Point out each Plasmodium parasite.
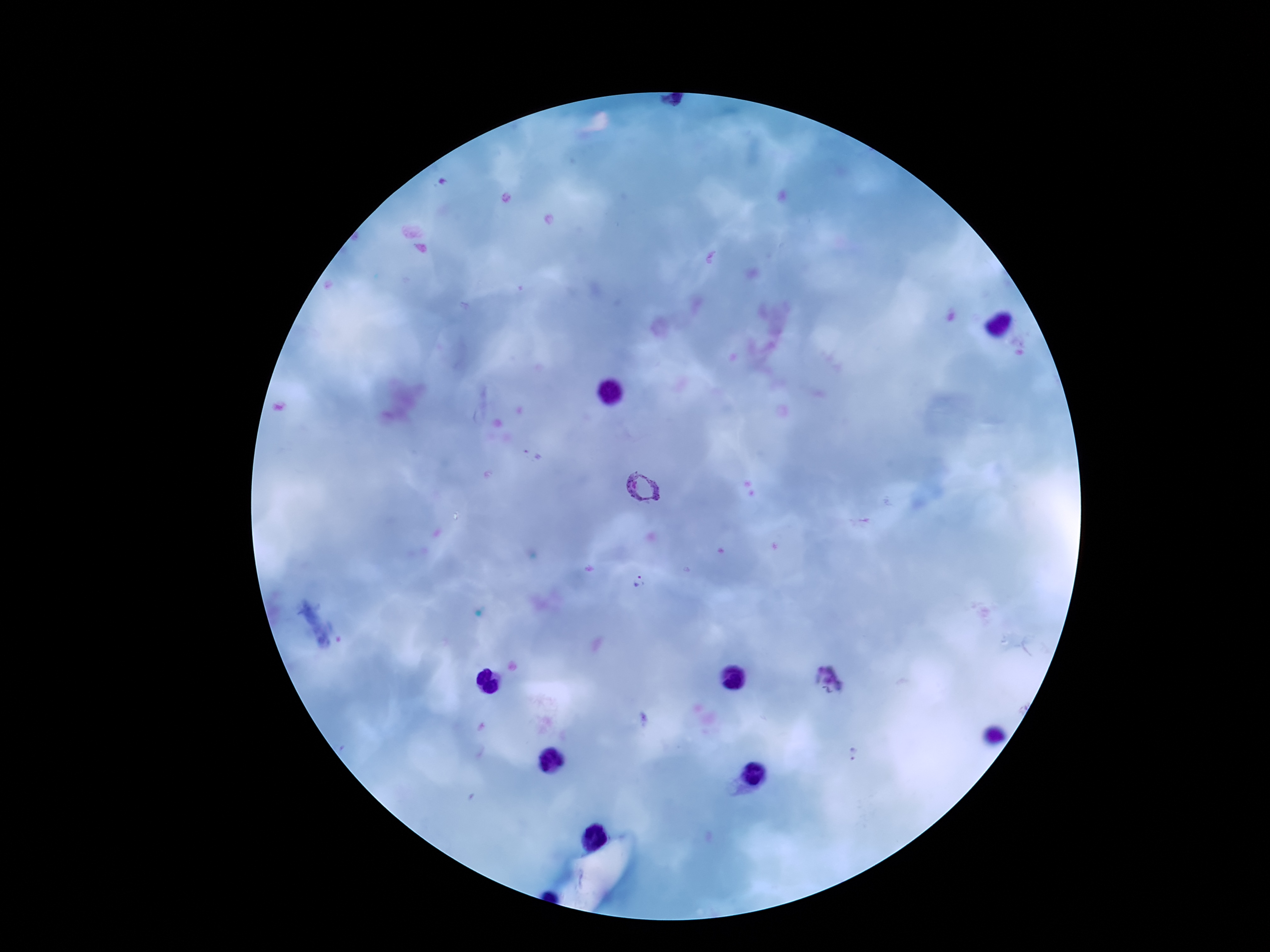
Approximate centers as [x, y] in pixels.
Plasmodium parasites: [645, 488], [641, 582], [829, 682], [855, 757].

Patient malaria status: positive. Thick blood smear. Single field of view. Giemsa stain. Image is 1270×952 pixels. Smartphone photograph taken through the microscope eyepiece. 100x magnification.